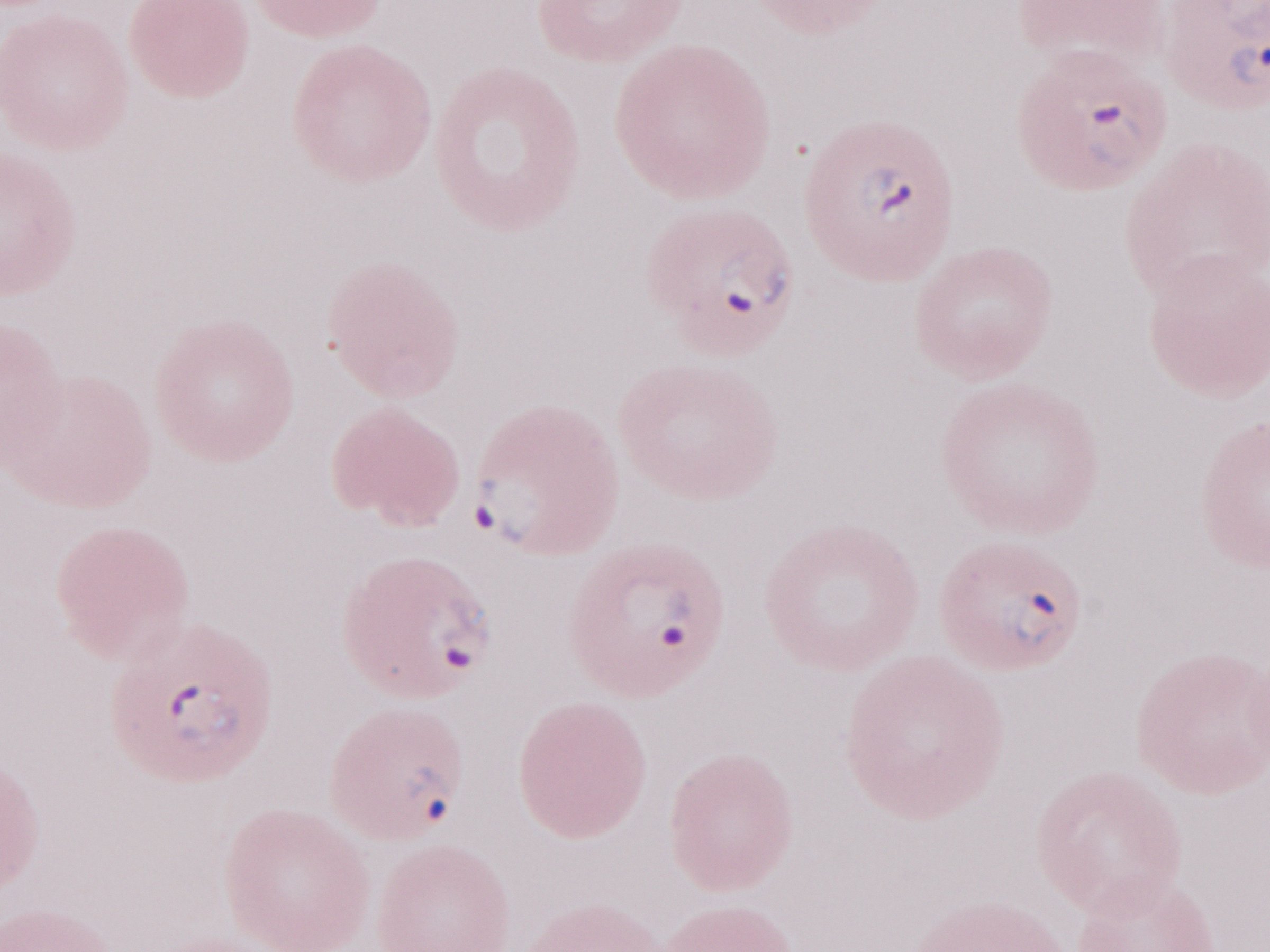 May-Grünwald-Giemsa stain. Olympus BX43 microscope and DP73 digital camera. 1,000x magnification. One field of this slide. Image is 1270×952 pixels. Thin blood film. Patient-level malaria diagnosis: positive.